Name the blood parasite species.
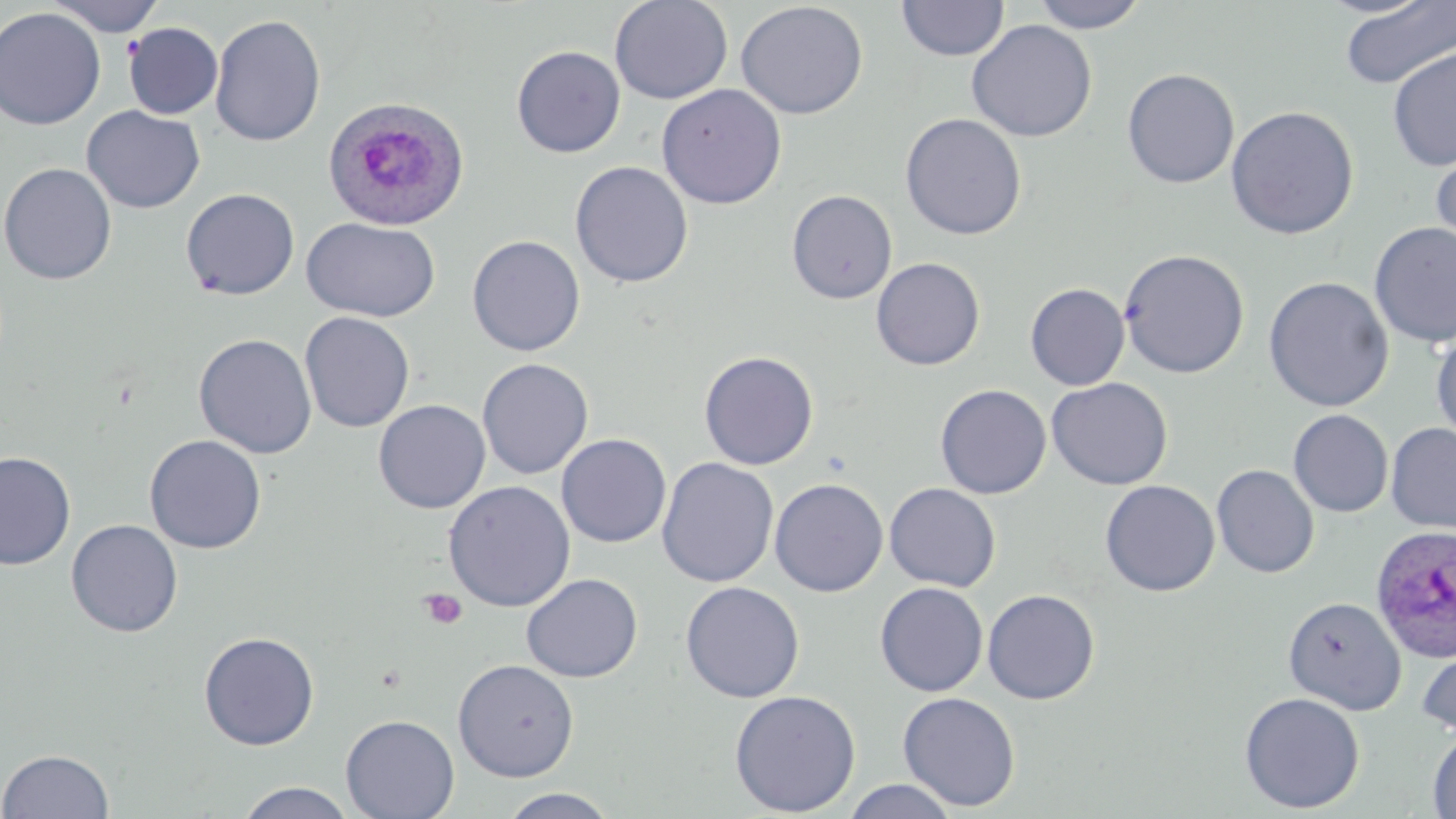

Plasmodium ovale.

Summary:
  - Coordinate format: approximate bounding boxes as [x1, y1, x2, y2] in pixels
  - Platelet locations: [418, 588, 468, 630]
  - Plasmodium ovale-infected red blood cell locations: [319, 99, 467, 234], [1370, 524, 1456, 661]
  - Uninfected red blood cell locations: [46, 0, 167, 37], [609, 0, 733, 105], [895, 0, 1009, 61], [1028, 0, 1151, 33], [735, 1, 869, 120], [1338, 1, 1456, 89], [0, 7, 106, 130], [210, 14, 326, 147], [966, 19, 1098, 142], [123, 22, 223, 120], [512, 45, 625, 158], [1387, 47, 1456, 172], [1121, 68, 1240, 188], [656, 83, 787, 209], [82, 105, 205, 214], [1225, 105, 1360, 240], [900, 113, 1027, 240], [1430, 144, 1456, 263], [570, 161, 693, 288], [0, 162, 117, 285], [180, 188, 300, 300], [786, 189, 898, 304], [300, 217, 441, 322], [1368, 222, 1456, 348], [466, 235, 586, 356], [1118, 248, 1250, 379], [870, 257, 986, 371], [1262, 276, 1395, 412], [1025, 283, 1130, 391], [299, 311, 415, 433], [1430, 328, 1456, 447], [193, 333, 317, 459], [699, 350, 819, 471], [476, 358, 594, 479], [1046, 377, 1172, 490], [934, 384, 1051, 499], [373, 399, 491, 513], [1288, 409, 1394, 517], [1386, 422, 1456, 534], [556, 433, 672, 548], [144, 435, 267, 554], [0, 451, 76, 570], [657, 457, 779, 587], [1211, 464, 1320, 578], [769, 478, 888, 597], [1100, 479, 1220, 596], [443, 480, 576, 612], [884, 482, 1001, 592], [66, 519, 183, 637], [521, 572, 643, 683], [680, 581, 805, 703], [875, 582, 988, 697], [982, 588, 1100, 705], [1283, 597, 1406, 715], [198, 631, 320, 750], [1417, 643, 1456, 738], [452, 658, 579, 782], [728, 689, 862, 816], [897, 691, 1021, 812], [1239, 691, 1365, 814], [340, 714, 459, 819], [1427, 727, 1456, 818], [0, 748, 114, 818], [841, 778, 960, 818], [235, 782, 357, 818], [496, 787, 622, 818]
  - Stain: May-Grünwald-Giemsa
  - Field of view: one of a larger specimen
  - Magnification: 1000x
  - Preparation: thin blood smear
  - Modality: light microscopy
  - Image size: 1456×819 pixels